Identify the cell.
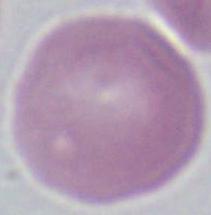

This is an erythrocyte.

Summary:
  - Magnification: 1000x
  - Modality: micrograph